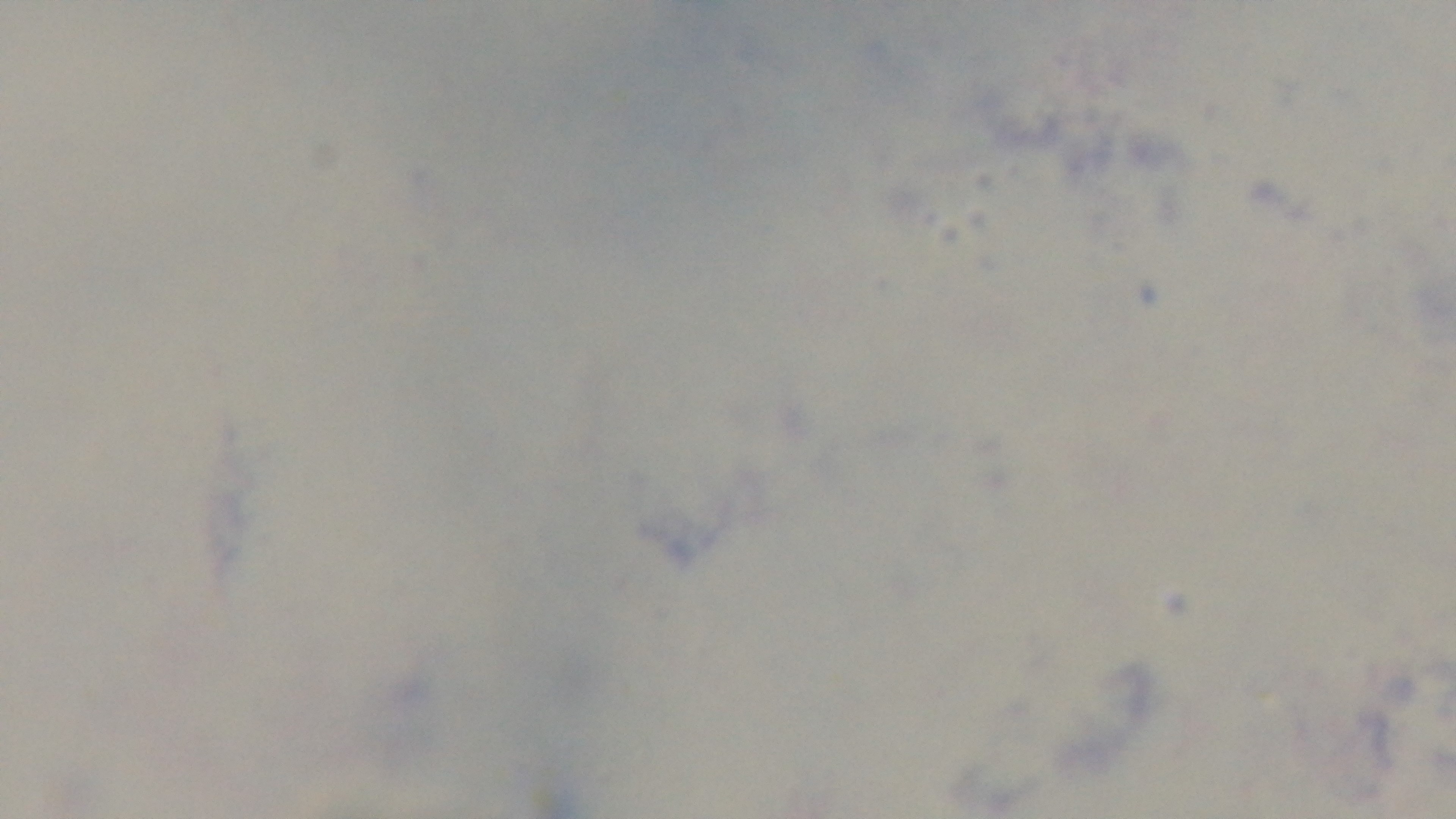

capture: mounted 4K digital camera
preparation: thick
field_of_view: one from the slide
objective: 100x oil immersion
modality: light microscopy
stain: Giemsa
malaria_status: uninfected